Name the parasite shown.
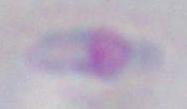

This is Toxoplasma gondii.

magnification = 1000x
modality = micrograph